State which parasite is depicted.
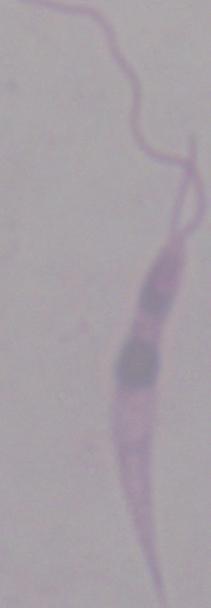
This is Leishmania.

magnification = 1000x
modality = micrograph